Report the malaria status of this cell.
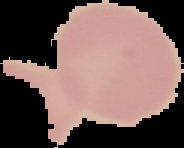
It is uninfected.

The area outside the segmented cell region is set to black. Image is 184×148 pixels. From a thin blood smear.